State which parasite is depicted.
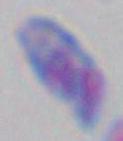

Toxoplasma gondii.

Micrograph. 1000x magnification.